State the preparation type.
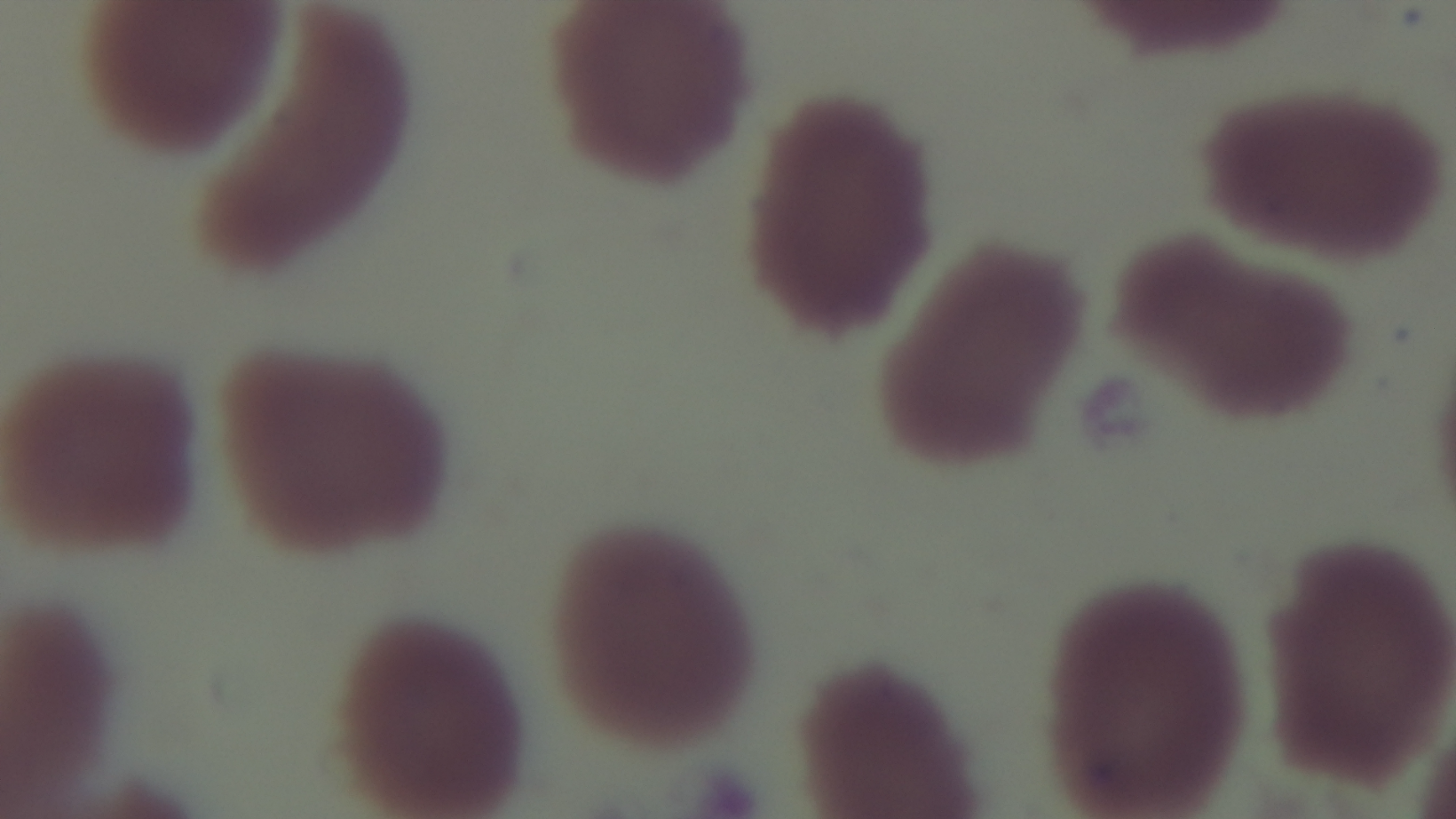
A thin smear.

Summary:
  - Objective: 100x oil immersion
  - Field of view: single
  - Capture: mounted 4K digital camera
  - Malaria status: uninfected
  - Modality: light microscopy
  - Stain: Giemsa